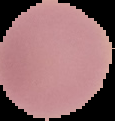
Summary:
  - Image size: 115×121 pixels
  - Result: no malaria parasites detected
  - Preparation: thin blood film
  - Image type: segmented cell region with the area outside set to black